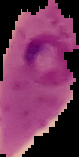
preparation: thin blood smear
image_size: 79×157 pixels
malaria_status: parasitized
image_type: cell region segmented out of the field of view; surrounding area masked to black